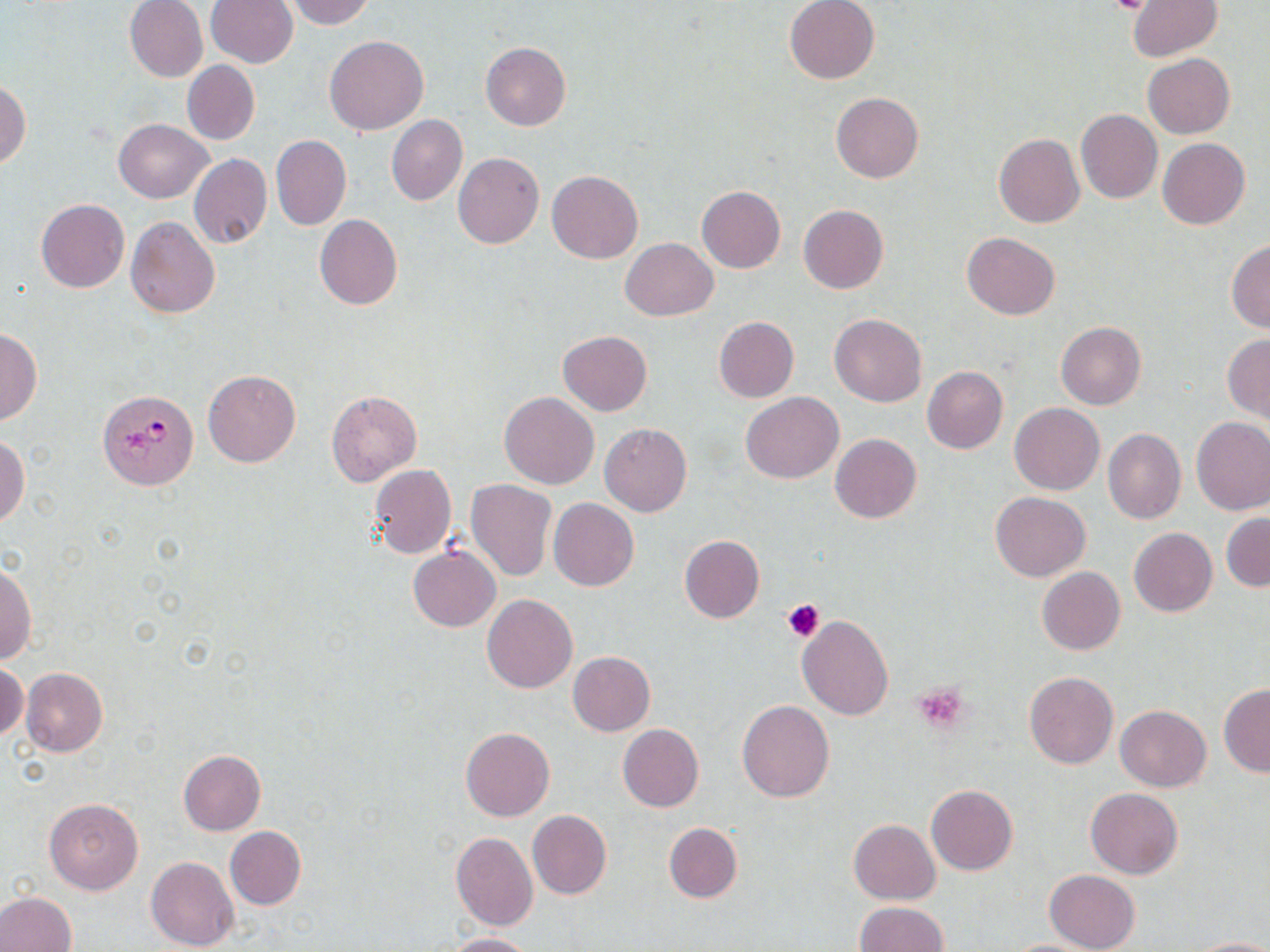

slide-level diagnosis = Plasmodium falciparum
stain = May-Grünwald-Giemsa
preparation = thin blood film
uninfected red blood cell locations = approximate bounding boxes as named x1/y1/x2/y2 corners in pixels: (x1=124, y1=0, x2=208, y2=82), (x1=205, y1=0, x2=297, y2=69), (x1=283, y1=0, x2=375, y2=28), (x1=784, y1=0, x2=879, y2=84), (x1=1128, y1=1, x2=1222, y2=60), (x1=325, y1=35, x2=428, y2=134), (x1=480, y1=42, x2=571, y2=131), (x1=1143, y1=54, x2=1234, y2=138), (x1=182, y1=60, x2=260, y2=145), (x1=0, y1=80, x2=31, y2=169), (x1=830, y1=92, x2=924, y2=184), (x1=1076, y1=109, x2=1162, y2=204), (x1=386, y1=115, x2=467, y2=206), (x1=113, y1=119, x2=211, y2=204), (x1=992, y1=132, x2=1085, y2=228), (x1=270, y1=135, x2=351, y2=231), (x1=1157, y1=138, x2=1250, y2=230), (x1=453, y1=152, x2=544, y2=249), (x1=188, y1=153, x2=272, y2=249), (x1=546, y1=171, x2=643, y2=264), (x1=697, y1=185, x2=786, y2=273), (x1=35, y1=199, x2=130, y2=293), (x1=798, y1=205, x2=890, y2=294), (x1=315, y1=214, x2=402, y2=310), (x1=125, y1=216, x2=219, y2=318), (x1=962, y1=232, x2=1059, y2=320), (x1=620, y1=238, x2=718, y2=321), (x1=1226, y1=240, x2=1270, y2=333), (x1=829, y1=313, x2=927, y2=407), (x1=714, y1=316, x2=798, y2=402), (x1=1056, y1=321, x2=1146, y2=410), (x1=0, y1=329, x2=42, y2=426), (x1=558, y1=331, x2=652, y2=416), (x1=1223, y1=334, x2=1270, y2=422), (x1=921, y1=366, x2=1008, y2=454), (x1=202, y1=368, x2=301, y2=467), (x1=326, y1=391, x2=422, y2=486), (x1=499, y1=392, x2=599, y2=489), (x1=740, y1=393, x2=842, y2=484), (x1=1010, y1=403, x2=1105, y2=495), (x1=1191, y1=416, x2=1270, y2=514), (x1=599, y1=423, x2=692, y2=517), (x1=1103, y1=428, x2=1186, y2=524), (x1=830, y1=433, x2=922, y2=523), (x1=0, y1=437, x2=29, y2=528), (x1=369, y1=464, x2=456, y2=559), (x1=466, y1=479, x2=557, y2=580), (x1=990, y1=491, x2=1090, y2=581), (x1=549, y1=498, x2=638, y2=592), (x1=1221, y1=513, x2=1270, y2=591), (x1=1129, y1=528, x2=1217, y2=618), (x1=678, y1=534, x2=765, y2=622), (x1=408, y1=545, x2=501, y2=631), (x1=0, y1=564, x2=37, y2=664), (x1=1037, y1=567, x2=1125, y2=655), (x1=481, y1=594, x2=577, y2=693), (x1=797, y1=616, x2=893, y2=720), (x1=568, y1=651, x2=655, y2=736), (x1=1, y1=662, x2=27, y2=743), (x1=20, y1=667, x2=108, y2=756), (x1=1023, y1=671, x2=1118, y2=769), (x1=1218, y1=684, x2=1270, y2=777), (x1=737, y1=700, x2=835, y2=802), (x1=1115, y1=705, x2=1211, y2=792), (x1=617, y1=724, x2=704, y2=812), (x1=460, y1=728, x2=555, y2=821), (x1=176, y1=750, x2=267, y2=835), (x1=926, y1=784, x2=1019, y2=875), (x1=1085, y1=787, x2=1183, y2=879), (x1=44, y1=798, x2=143, y2=894), (x1=528, y1=809, x2=610, y2=899), (x1=848, y1=819, x2=940, y2=904), (x1=664, y1=822, x2=742, y2=903), (x1=224, y1=827, x2=306, y2=910), (x1=450, y1=832, x2=539, y2=931), (x1=145, y1=856, x2=239, y2=951), (x1=1044, y1=869, x2=1141, y2=952), (x1=0, y1=891, x2=76, y2=951), (x1=854, y1=901, x2=948, y2=952), (x1=437, y1=932, x2=535, y2=951), (x1=1189, y1=936, x2=1270, y2=952), (x1=999, y1=939, x2=1104, y2=952)
field of view = single
platelet locations = approximate bounding boxes as named x1/y1/x2/y2 corners in pixels: (x1=1103, y1=0, x2=1156, y2=15), (x1=783, y1=599, x2=824, y2=642), (x1=912, y1=681, x2=971, y2=733)
Plasmodium falciparum-infected red blood cell locations = approximate bounding boxes as named x1/y1/x2/y2 corners in pixels: (x1=97, y1=389, x2=199, y2=490)
image size = 1270×952 pixels
magnification = 1000x
modality = optical microscopy